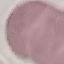
Malaria status: uninfected. Automatically extracted cell patch, resized to 64 × 64 pixels. Thin blood film. Acquired by smartphone through the microscope eyepiece. Giemsa-stained preparation.